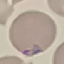
result = malaria parasites detected
stain = Giemsa
capture = smartphone through the microscope eyepiece
preparation = thin blood film
image type = cell patch, automatically extracted from a larger field of view and resized to 64 × 64 pixels